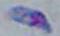

magnification = 1000x
modality = micrograph
identification = Toxoplasma gondii